Assess the morphology of the erythrocytes.
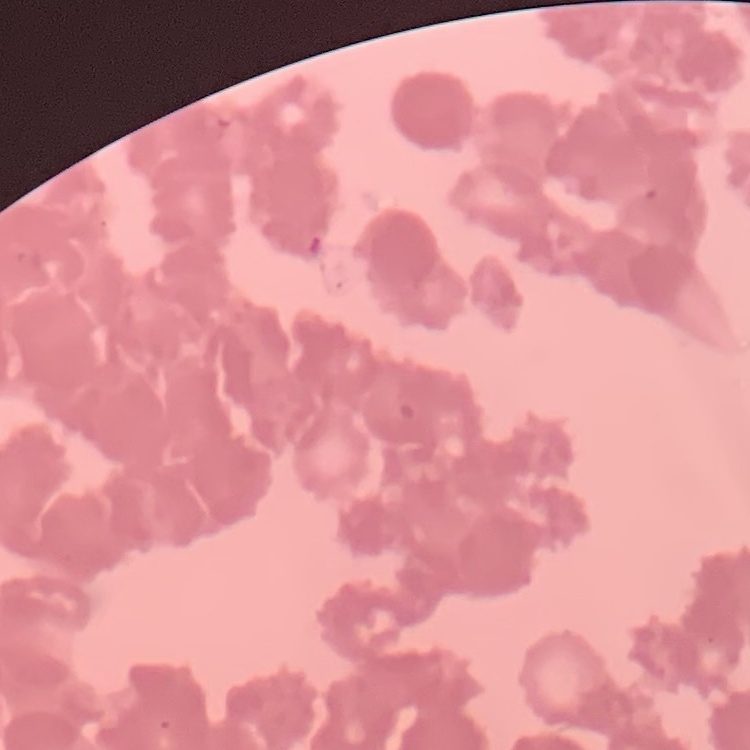
Rouleaux formation.

Summary:
  - Stain: Field's or Giemsa
  - Preparation: thin blood smear
  - Image type: one tile cut from a larger photomicrograph